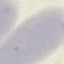
Malaria status: uninfected. Photographed with a smartphone camera at the microscope eyepiece. Thin blood smear. Giemsa-stained preparation. Automatically extracted cell patch, resized to 64 × 64 pixels.